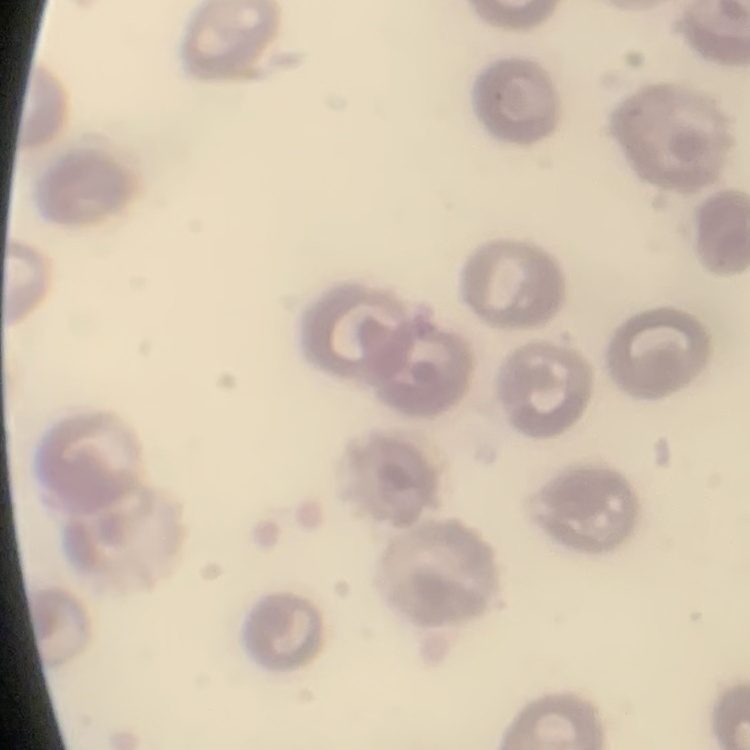

red blood cell morphology = no rouleaux formation
image type = square crop of a larger photomicrograph
stain = Field's or Giemsa
preparation = thin peripheral smear